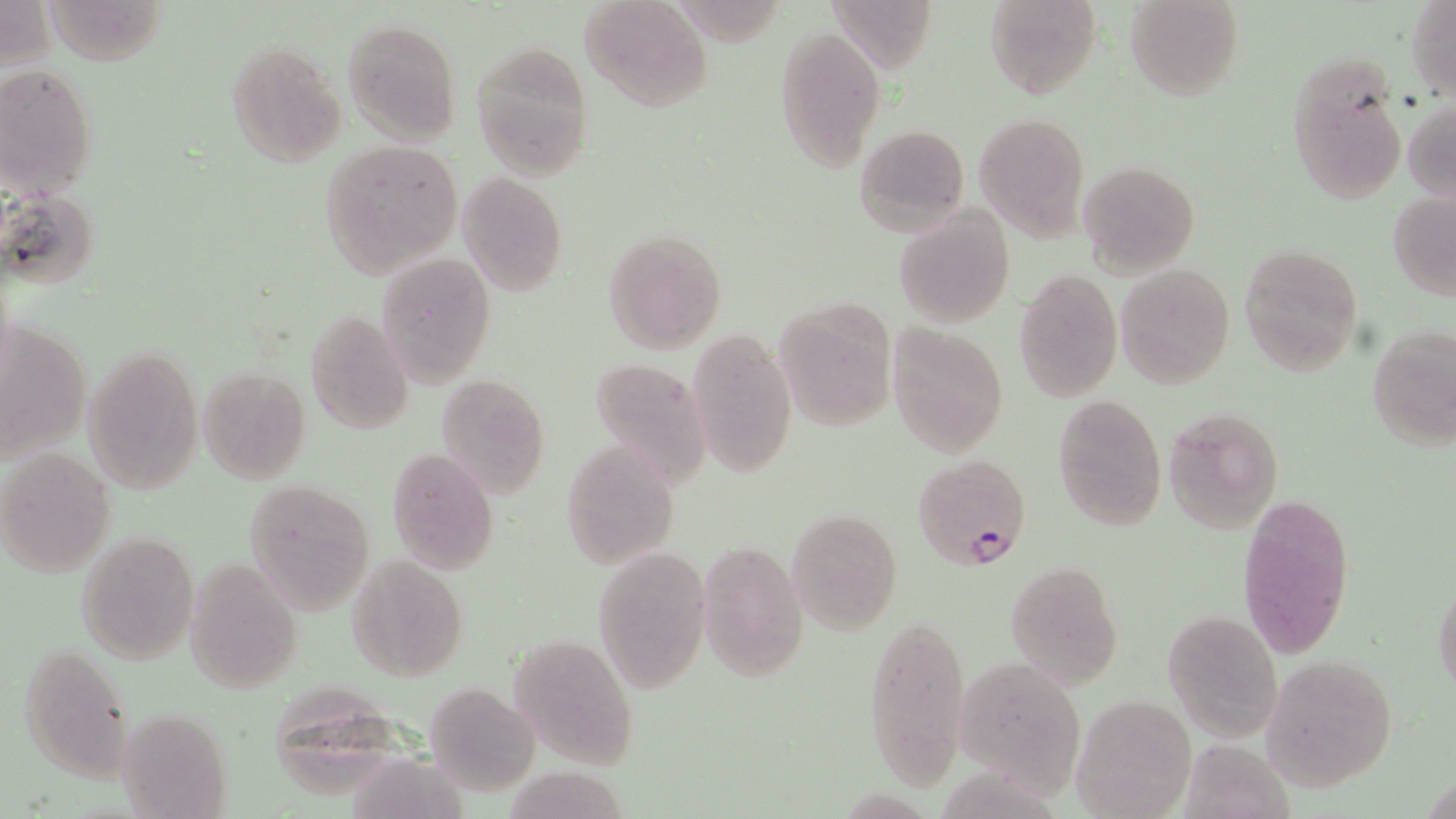

slide_level_diagnosis: Plasmodium falciparum
preparation: thin blood film
plasmodium_falciparum_infected_red_blood_cell_locations: 'approximate bounding boxes as (x1,y1)-(x2,y2) corner pairs in pixels: (911,453)-(1032,571)'
stain: May-Grünwald-Giemsa
magnification: 1000x
field_of_view: one of a larger specimen
image_size: 1456×819 pixels
modality: light microscopy
uninfected_red_blood_cell_locations: 'approximate bounding boxes as (x1,y1)-(x2,y2) corner pairs in pixels: (578,0)-(712,112), (828,0)-(938,72), (985,0)-(1102,100), (1126,0)-(1245,101), (1407,1)-(1455,100), (342,15)-(463,147), (772,24)-(884,173), (471,39)-(596,179), (224,40)-(346,168), (1285,52)-(1409,204), (0,64)-(99,198), (1404,100)-(1456,199), (975,112)-(1091,240), (854,124)-(969,236), (317,141)-(463,278), (1078,160)-(1199,277), (456,173)-(569,295), (0,186)-(102,292), (1388,187)-(1456,301), (894,204)-(1016,327), (603,227)-(726,353), (1238,244)-(1363,375), (375,252)-(497,389), (1116,263)-(1234,389), (1014,269)-(1123,402), (773,297)-(899,432), (304,309)-(414,434), (1,315)-(95,464), (887,321)-(1010,458), (1366,324)-(1456,452), (687,325)-(797,479), (81,344)-(205,494), (586,358)-(713,488), (197,365)-(312,484), (436,372)-(550,499), (1052,395)-(1168,532), (1164,406)-(1285,534), (561,439)-(681,570), (0,445)-(116,578), (387,447)-(499,573), (244,478)-(377,613), (1237,493)-(1355,660), (786,507)-(902,634), (76,533)-(199,664), (696,540)-(809,683), (591,544)-(711,694), (348,555)-(469,680), (184,556)-(304,694), (1005,561)-(1124,688), (1432,581)-(1456,696), (1162,608)-(1283,741), (864,613)-(971,790), (508,634)-(639,771), (20,640)-(135,786), (1263,653)-(1397,790), (957,655)-(1087,798), (424,681)-(540,795), (264,684)-(402,791), (1070,693)-(1200,817), (114,708)-(232,818), (1178,735)-(1304,819), (336,751)-(469,815), (508,753)-(623,818)'